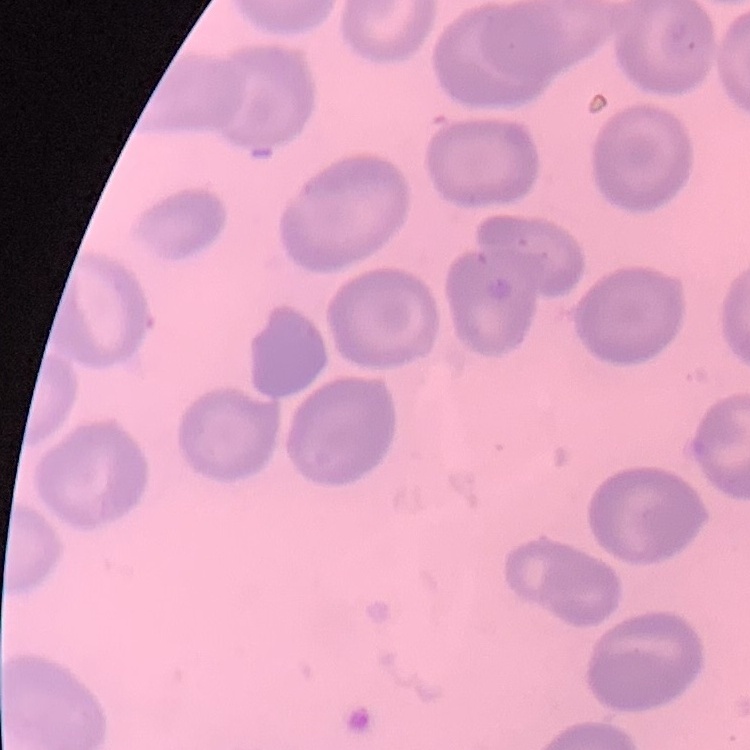 The red blood cells show no rouleaux formation. Square crop of a larger photomicrograph. Stained with either Field's or Giemsa. Thin peripheral smear.